Identify the parasite.
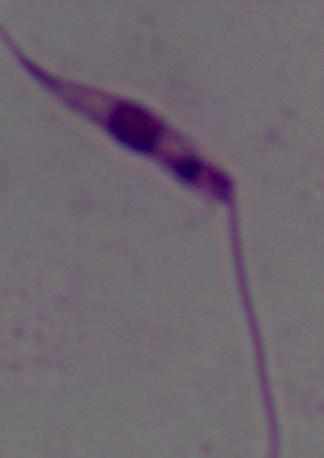
This is Leishmania.

1000x magnification. Micrograph.